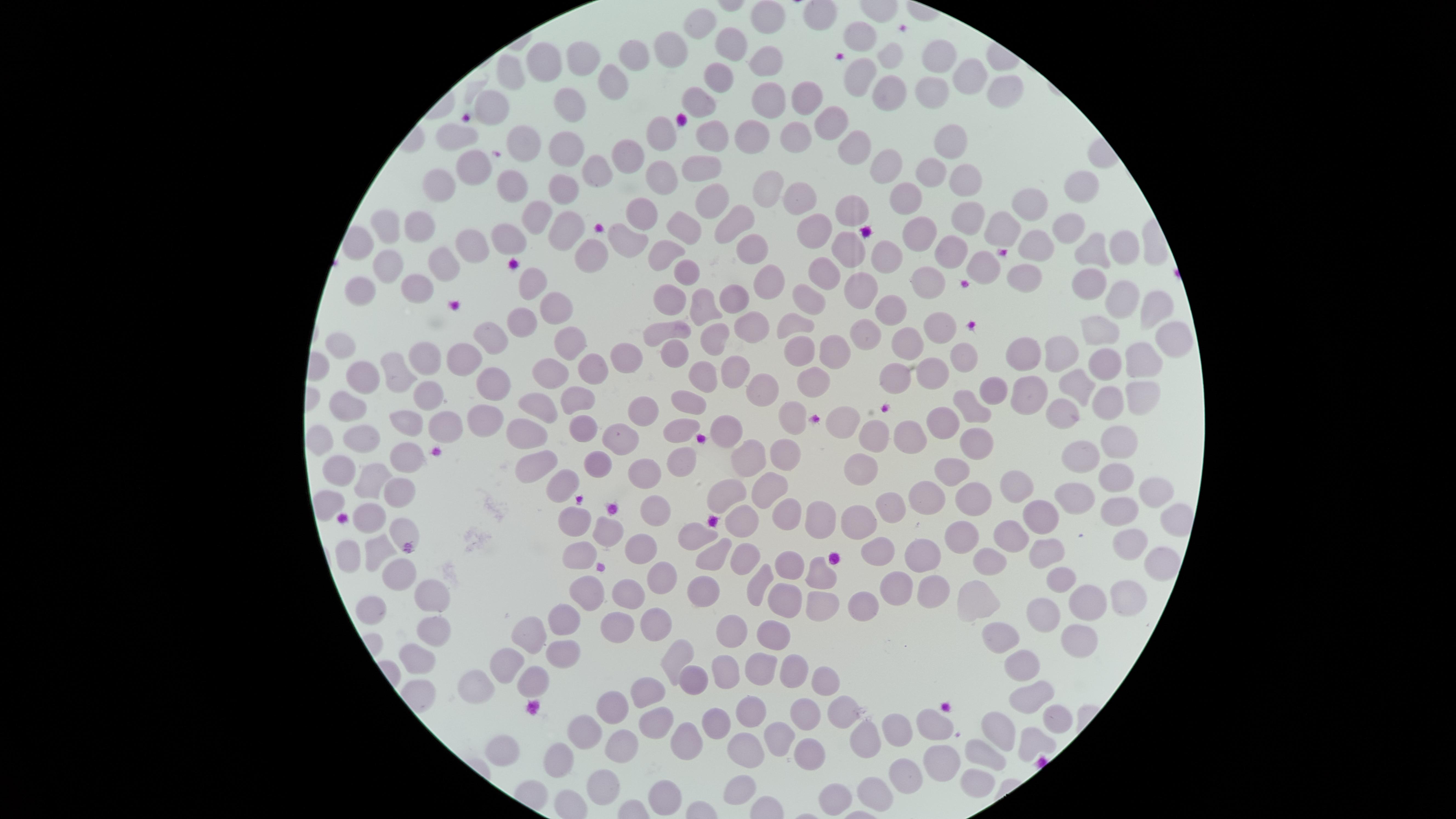
{
  "presence": "no malaria parasites detected",
  "visible_region": "circular",
  "field_of_view": "single",
  "image_size": "1456×819 pixels",
  "capture": "smartphone photograph through the microscope eyepiece",
  "uninfected_red_blood_cells": "approximate marker points, in pixels from the top-left corner: (x=768, y=17), (x=699, y=26), (x=859, y=36), (x=729, y=44), (x=669, y=45), (x=888, y=51), (x=938, y=53), (x=631, y=55), (x=763, y=55), (x=582, y=57), (x=543, y=62), (x=511, y=69), (x=717, y=77), (x=970, y=78), (x=613, y=79), (x=858, y=79), (x=887, y=86), (x=935, y=86), (x=1007, y=91), (x=796, y=92), (x=695, y=102), (x=492, y=104), (x=567, y=106), (x=756, y=107), (x=834, y=122), (x=716, y=131), (x=458, y=133), (x=752, y=134), (x=788, y=135), (x=658, y=137), (x=520, y=141), (x=849, y=142), (x=949, y=142), (x=560, y=145), (x=628, y=152), (x=882, y=165), (x=476, y=166), (x=594, y=166), (x=931, y=167), (x=705, y=168), (x=437, y=178), (x=964, y=180), (x=511, y=185), (x=559, y=186), (x=658, y=186), (x=765, y=186), (x=1081, y=189), (x=718, y=193), (x=909, y=193), (x=797, y=199), (x=850, y=208), (x=1020, y=208), (x=534, y=212), (x=640, y=212), (x=387, y=220), (x=964, y=222), (x=735, y=223), (x=678, y=225), (x=995, y=225), (x=421, y=226), (x=559, y=226), (x=1066, y=227), (x=817, y=232), (x=918, y=232), (x=511, y=237), (x=627, y=238), (x=468, y=242), (x=1039, y=243), (x=1123, y=244), (x=847, y=247), (x=1092, y=248), (x=752, y=251), (x=959, y=251), (x=885, y=253), (x=669, y=254), (x=590, y=259), (x=992, y=259), (x=387, y=261), (x=440, y=265), (x=685, y=274), (x=821, y=274), (x=1023, y=276), (x=929, y=277), (x=1090, y=279), (x=535, y=280), (x=769, y=282), (x=857, y=288), (x=420, y=289), (x=361, y=291), (x=669, y=294), (x=1117, y=296), (x=733, y=298), (x=803, y=298), (x=558, y=304), (x=702, y=306), (x=1148, y=306), (x=894, y=310), (x=527, y=312), (x=789, y=318), (x=942, y=323), (x=752, y=327), (x=1101, y=331), (x=656, y=332), (x=860, y=332), (x=487, y=334), (x=1166, y=334), (x=716, y=335), (x=907, y=337), (x=570, y=339), (x=340, y=343), (x=835, y=347), (x=1060, y=349), (x=1027, y=350), (x=672, y=353), (x=960, y=353), (x=797, y=354), (x=426, y=359), (x=623, y=359), (x=1141, y=361), (x=457, y=362), (x=1101, y=363), (x=586, y=366), (x=732, y=366), (x=551, y=369), (x=931, y=371), (x=398, y=374), (x=360, y=375), (x=699, y=376), (x=897, y=376), (x=813, y=377), (x=490, y=380), (x=768, y=386), (x=1079, y=386), (x=992, y=387), (x=429, y=393), (x=1027, y=395), (x=581, y=397), (x=1140, y=398), (x=536, y=402), (x=690, y=402), (x=970, y=403), (x=346, y=404), (x=1105, y=404), (x=637, y=406), (x=1059, y=408), (x=477, y=416), (x=790, y=417), (x=408, y=418), (x=840, y=418), (x=440, y=420), (x=944, y=423), (x=581, y=425), (x=526, y=427), (x=684, y=427), (x=727, y=427), (x=871, y=431), (x=904, y=434), (x=975, y=435), (x=360, y=440), (x=620, y=440), (x=319, y=441), (x=1123, y=443), (x=1078, y=449), (x=782, y=450), (x=752, y=452), (x=538, y=459), (x=680, y=460), (x=860, y=460), (x=408, y=462), (x=593, y=463), (x=340, y=467), (x=949, y=468), (x=644, y=472), (x=371, y=477), (x=1109, y=477), (x=770, y=484), (x=1019, y=484), (x=558, y=486), (x=395, y=488), (x=1154, y=491), (x=727, y=493), (x=927, y=493), (x=1067, y=497), (x=962, y=499), (x=334, y=503), (x=655, y=507), (x=790, y=507), (x=893, y=507), (x=1117, y=511), (x=574, y=512), (x=1045, y=516), (x=371, y=520), (x=818, y=520), (x=857, y=520), (x=740, y=522), (x=602, y=524), (x=400, y=529), (x=697, y=532), (x=957, y=534), (x=999, y=535), (x=1120, y=539), (x=378, y=544), (x=640, y=546), (x=919, y=548), (x=1051, y=548), (x=874, y=550), (x=717, y=555), (x=349, y=556), (x=582, y=556), (x=742, y=556), (x=986, y=560), (x=784, y=565), (x=1157, y=565), (x=395, y=571), (x=815, y=573), (x=1056, y=573), (x=661, y=575), (x=759, y=579), (x=592, y=584), (x=895, y=587), (x=701, y=591), (x=1124, y=591), (x=623, y=592), (x=931, y=593), (x=973, y=594), (x=435, y=595), (x=1081, y=597), (x=856, y=599), (x=813, y=601), (x=782, y=605), (x=1038, y=612), (x=373, y=613), (x=656, y=618), (x=563, y=620), (x=430, y=626), (x=614, y=628), (x=727, y=628), (x=1007, y=635), (x=770, y=636), (x=531, y=638), (x=1073, y=638), (x=411, y=655), (x=563, y=656), (x=676, y=656), (x=1024, y=661), (x=506, y=665), (x=726, y=667), (x=759, y=667), (x=795, y=670), (x=534, y=682), (x=478, y=686), (x=688, y=686), (x=821, y=691), (x=1032, y=691), (x=645, y=695), (x=609, y=702), (x=749, y=709), (x=800, y=711), (x=714, y=712), (x=844, y=712), (x=1050, y=717), (x=586, y=719), (x=998, y=719), (x=932, y=720), (x=648, y=723), (x=899, y=729), (x=776, y=737), (x=627, y=738), (x=869, y=738), (x=681, y=741), (x=1032, y=741), (x=740, y=746), (x=502, y=751), (x=808, y=752), (x=977, y=752), (x=551, y=755), (x=939, y=760), (x=904, y=776), (x=975, y=776), (x=598, y=780), (x=744, y=781), (x=873, y=785), (x=666, y=790), (x=821, y=796)",
  "stain": "Giemsa",
  "preparation": "thin smear of blood"
}